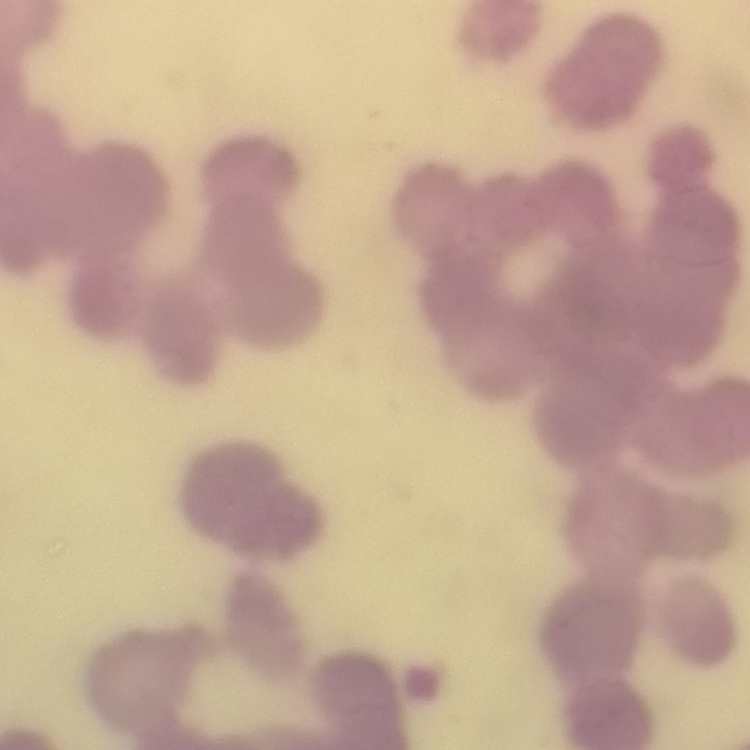

The red blood cells show rouleaux formation. Field's or Giemsa stain. Thin blood smear. One tile cut from a larger photomicrograph.